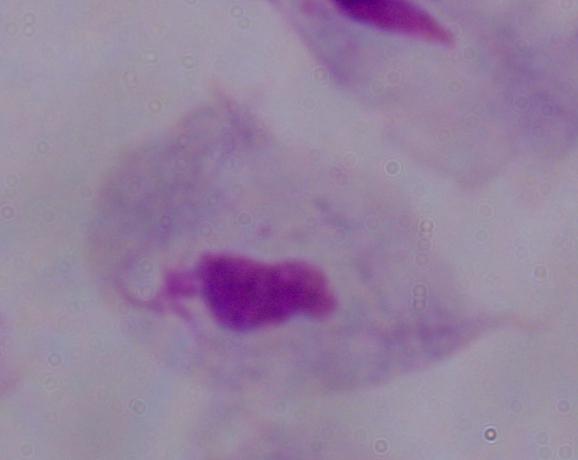

A trichomonad is shown. Captured at 1000x magnification. Micrograph.